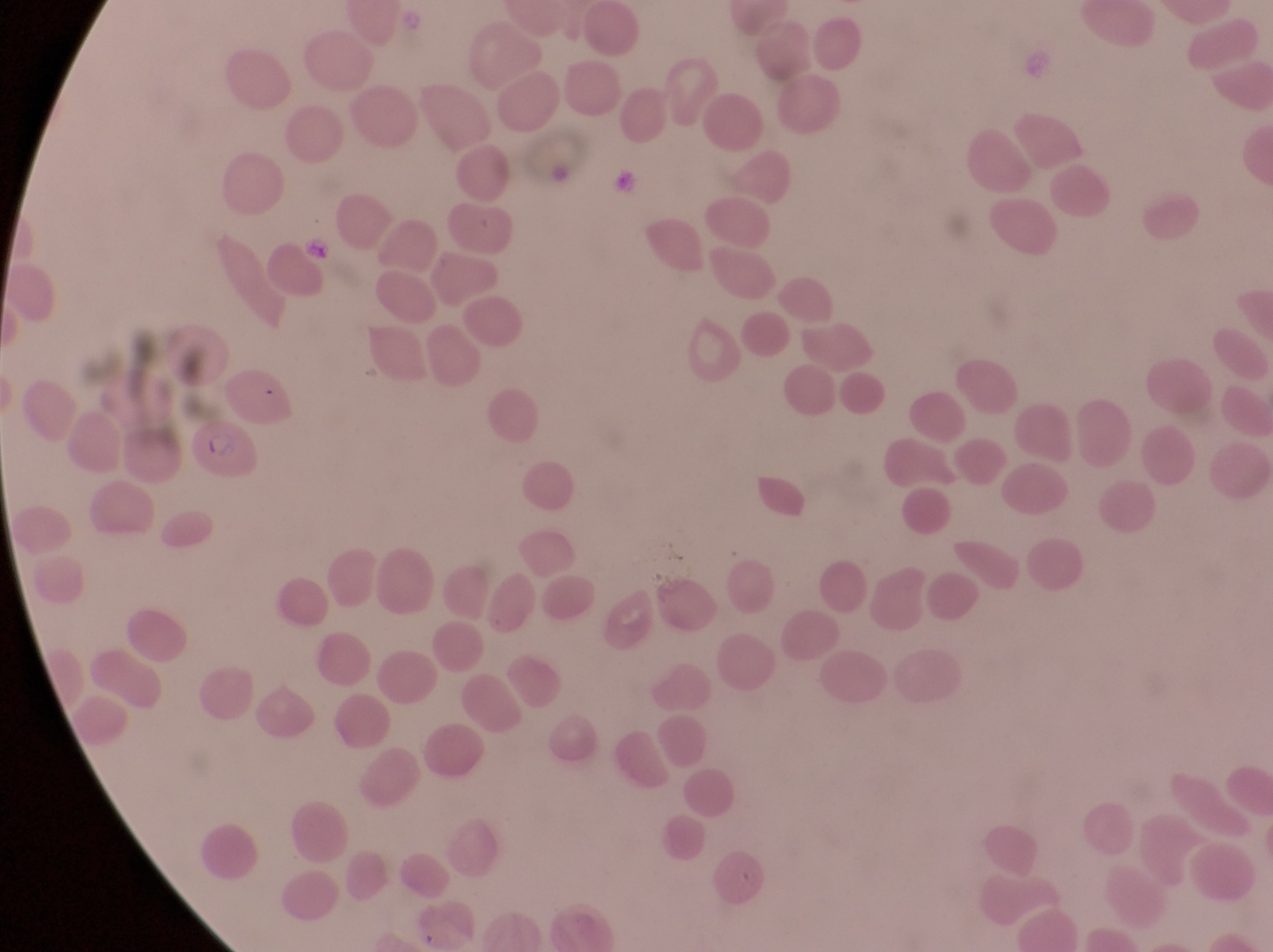
image_size: 1273×952 pixels
capture: smartphone photograph through the eyepiece of an Olympus CX-23 microscope
magnification: 1000x
parasitised_red_blood_cell_locations: 'approximate bounding boxes as left top right bottom in pixels: 192 415 262 485'
field_of_view: single
country: Uganda
artifact_platelet_like_body_stain_precipitate_or_debris_locations: 'approximate bounding boxes as left top right bottom in pixels: 610 167 642 200; 304 231 337 260'
preparation: thin blood smear